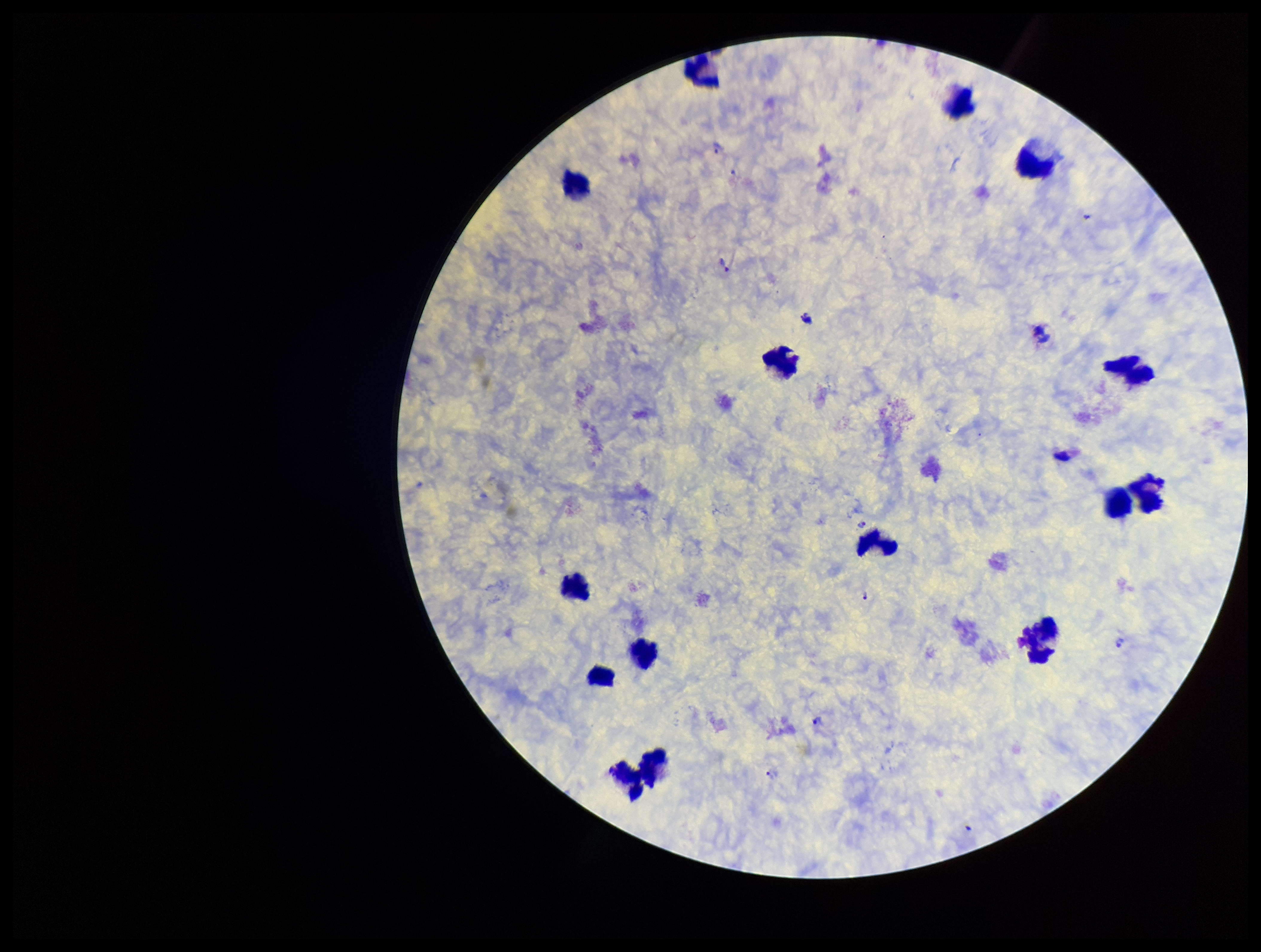
capture = smartphone photograph through the microscope eyepiece
leukocyte count = 15
image size = 1261×952 pixels
stain = Giemsa
Plasmodium parasites = detected
patient malaria status = positive
species reported for this patient = Plasmodium vivax
preparation = thick blood smear
field of view = one from this slide
parasite count = 6